Describe the morphology of the red blood cells.
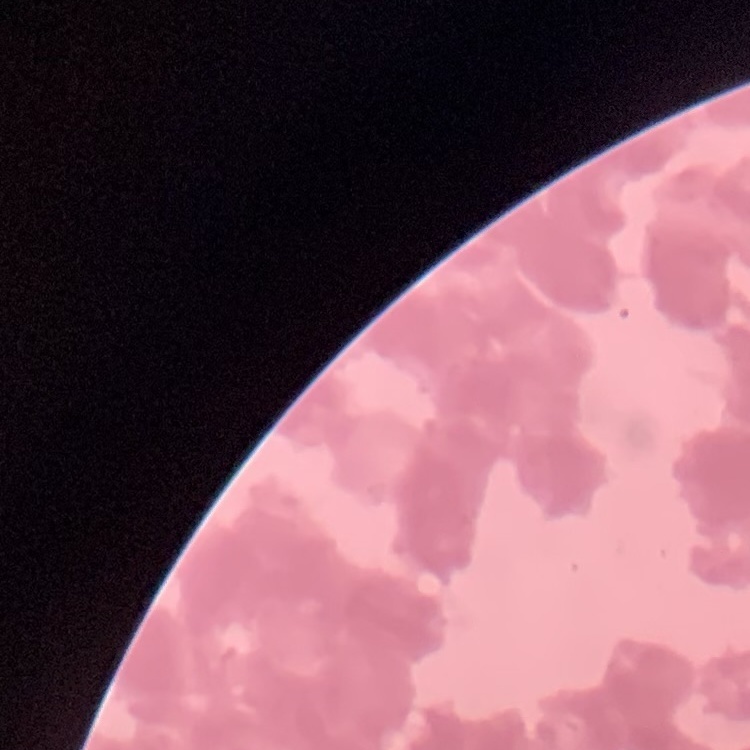
They show rouleaux formation.

Stained with either Field's or Giemsa. One tile cut from a larger photomicrograph. Thin blood smear.